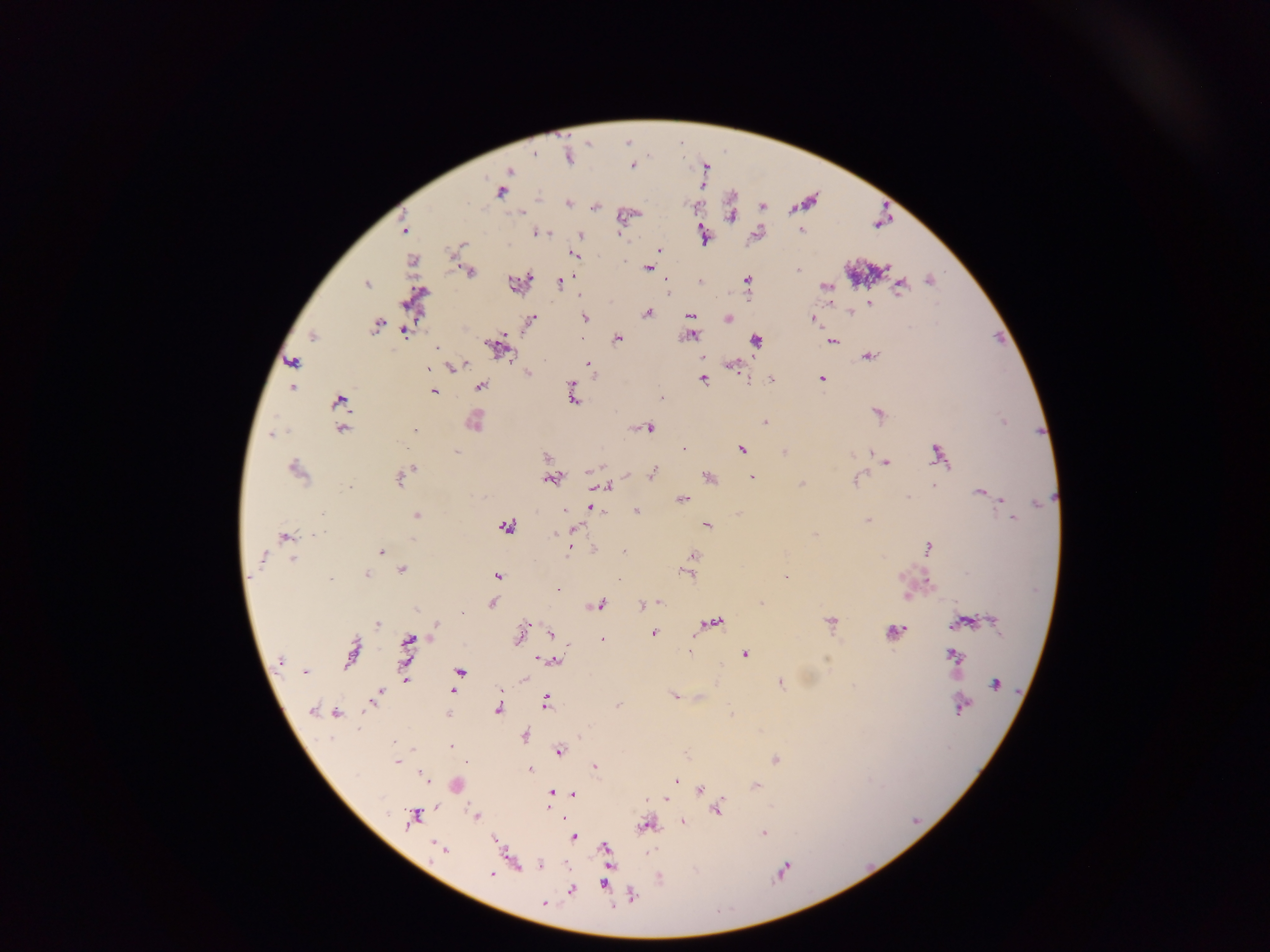

Approximate centers as x y in pixels. Plasmodium parasite locations: 568 156; 632 166; 509 171; 501 192; 567 203; 521 212; 730 216; 403 230; 801 231; 540 232; 580 235; 704 236; 461 245; 659 250; 573 255; 412 261; 647 268; 797 270; 471 272; 747 279; 929 279; 560 282; 514 283; 366 285; 824 286; 900 286; 870 304; 851 313; 647 314; 691 315; 728 318; 812 318; 585 319; 531 320; 375 326; 405 331; 313 336; 691 336; 618 339; 756 340; 832 341; 436 347; 496 348; 869 356; 292 361; 588 363; 454 366; 734 367; 428 369; 529 373; 821 379; 703 380; 772 380; 480 386; 292 387; 572 388; 434 391; 573 398; 660 398; 339 401; 878 414; 474 421; 1004 421; 764 422; 650 428; 415 429; 343 430; 272 435; 684 449; 741 449; 456 452; 784 452; 871 453; 938 454; 547 456; 887 463; 413 468; 296 471; 653 474; 709 477; 752 477; 399 479; 551 480; 855 481; 802 484; 933 485; 606 486; 349 487; 979 493; 990 495; 908 497; 682 499; 1000 499; 1039 503; 593 508; 599 510; 565 511; 637 511; 321 515; 416 516; 1011 519; 868 521; 707 525; 506 526; 573 529; 318 533; 555 533; 815 535; 285 536; 412 541; 928 548; 381 551; 568 552; 693 556; 263 559; 292 559; 401 570; 687 573; 367 575; 497 576; 785 576; 929 581; 557 589; 906 596; 661 603; 762 603; 492 604; 601 605; 642 605; 462 613; 994 620; 830 622; 960 622; 715 623; 378 624; 436 629; 895 632; 551 633; 653 633; 520 635; 602 639; 408 643; 352 652; 745 653; 953 656; 542 659; 280 660; 553 660; 459 671; 305 672; 406 679; 781 683; 995 684; 453 691; 674 696; 375 698; 546 701; 371 702; 618 705; 960 707; 498 710; 312 711; 337 714; 447 714; 524 736; 451 746; 559 751; 774 760; 397 762; 465 762; 594 768; 530 769; 424 776; 677 780; 757 785; 700 789; 551 793; 574 794; 666 799; 717 809; 413 817; 477 817; 682 821; 646 825; 763 833; 573 837; 438 847; 606 848; 442 849; 540 865; 782 871; 492 874; 604 884; 572 891; 632 895; 545 903. Photographed through a microscope with a mobile-phone camera. Thick blood film. Sample from Ghana. Image is 1270×952 pixels. Single field of view.